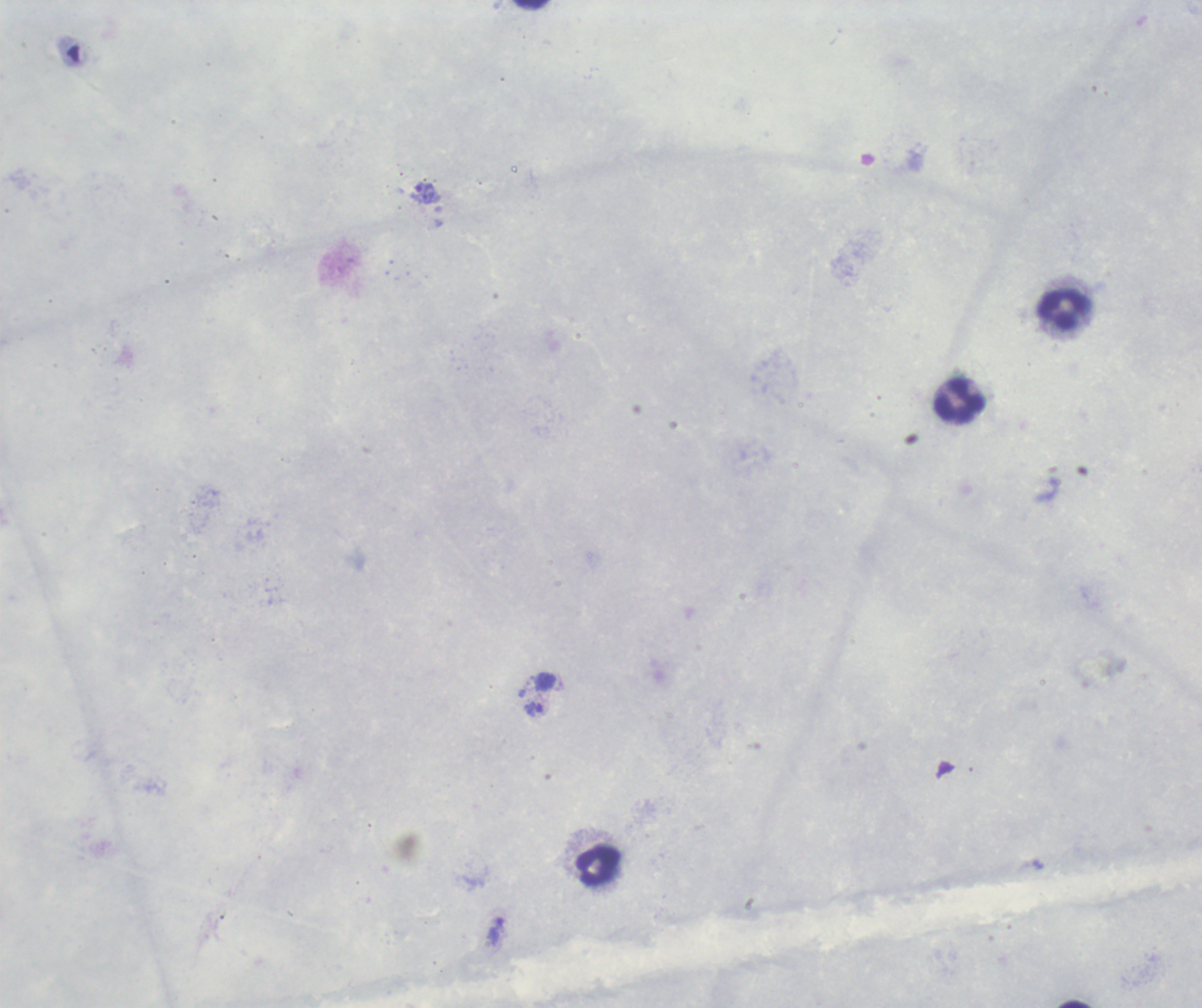

context: previously used in an actual diagnosis
field_of_view: one from this slide
image_size: 1202×1008 pixels
preparation: thick blood smear
leukocyte_locations: 'approximate centers as {x, y} in pixels: {1064, 310}, {959, 402}, {598, 867}'
background_quality: poor
trophozoite_locations: 'approximate centers as {x, y} in pixels: {425, 192}, {535, 711}, {495, 930}'
result: Plasmodium parasites identified
magnification: 100x
stain: Romanowsky